Give the position of every Plasmodium falciparum parasite, noting its life-cycle stage.
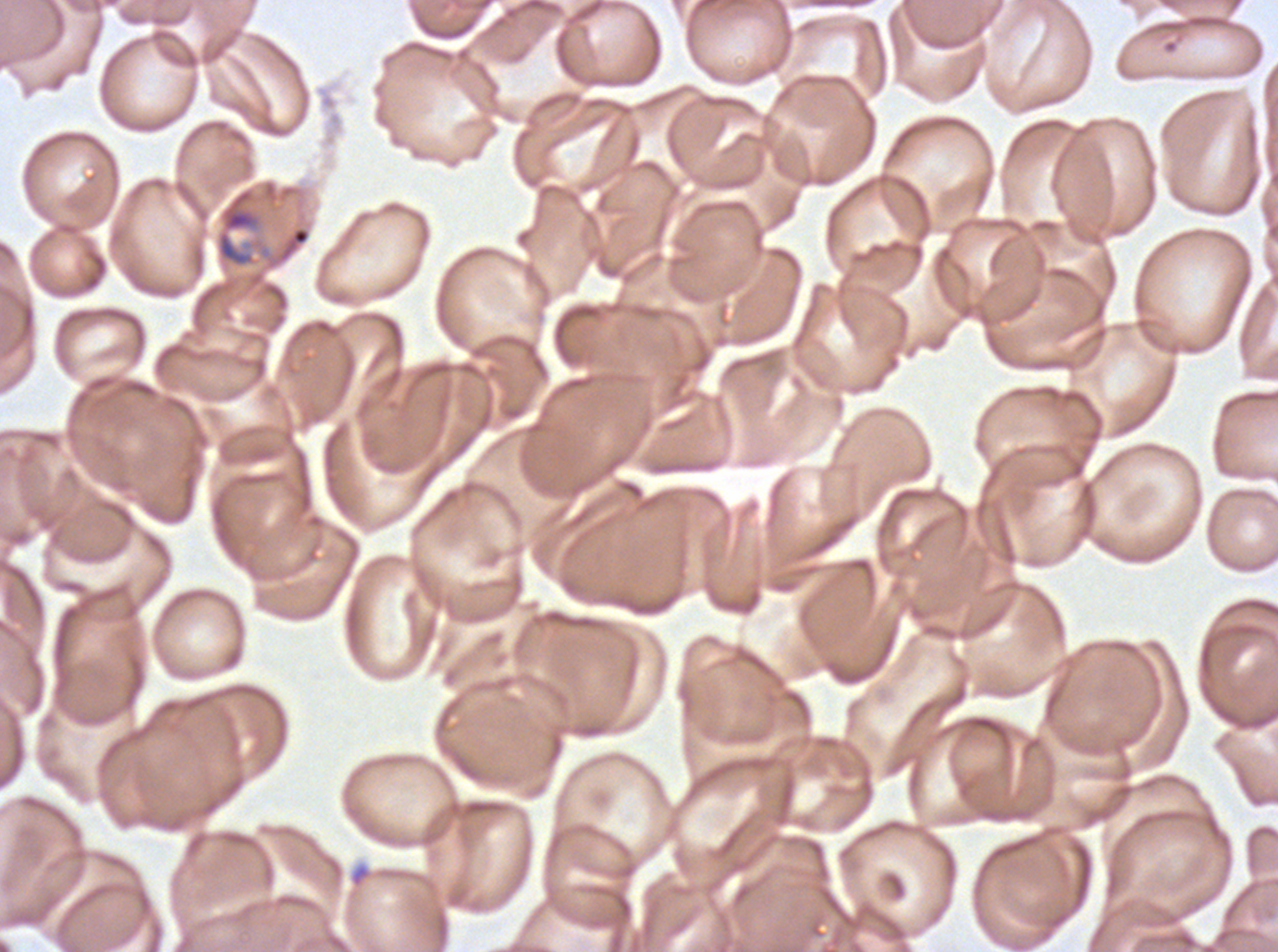
Approximate bounding rectangles given as corner coordinates in pixels from the top-left.
Mid trophozoites: (x1=216, y1=188, x2=260, y2=267).
No rings, late-ring/early-trophozoite forms, late trophozoites, early schizonts, late schizonts, segmenters, or gametocytes observed.

stain = Giemsa
preparation = thin blood film
specimen = ex-vivo Plasmodium falciparum culture from a patient in The Gambia, grown for 24 to 48 hours
field of view = sub-image separated from a larger composite
image size = 1278×952 pixels